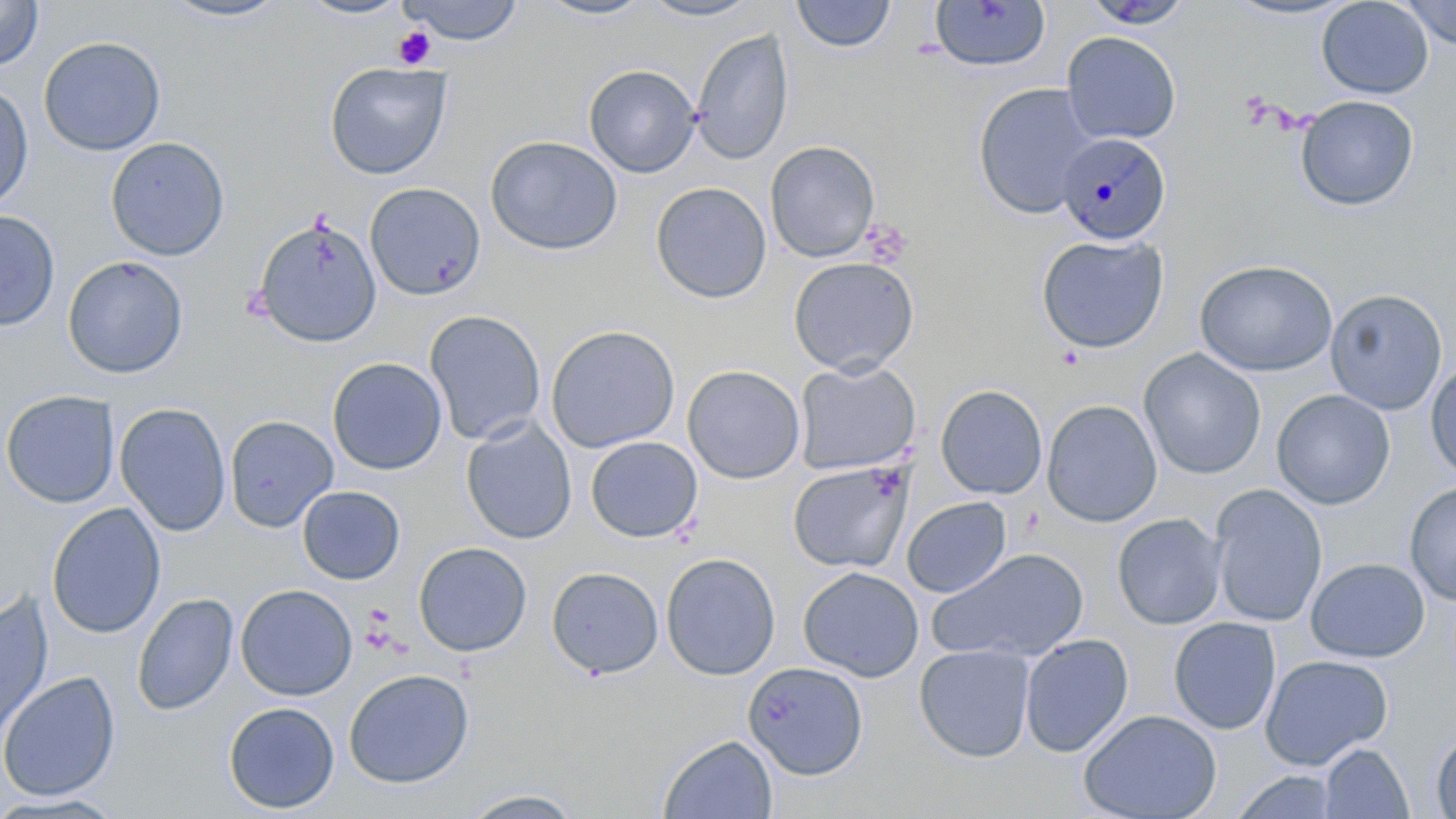

Summary:
  - Coordinate format: approximate bounding boxes as [x1, y1, x2, y2] in pixels
  - Platelet locations: [392, 26, 436, 70], [864, 220, 912, 266], [361, 609, 397, 653]
  - Uninfected red blood cell locations: [296, 0, 411, 20], [1220, 0, 1360, 22], [1317, 0, 1434, 99], [0, 1, 44, 71], [156, 1, 294, 23], [398, 1, 525, 45], [531, 1, 655, 22], [637, 1, 763, 22], [791, 1, 898, 54], [1080, 1, 1196, 29], [928, 2, 1052, 73], [1402, 2, 1456, 48], [691, 27, 794, 165], [1061, 31, 1182, 145], [38, 35, 166, 156], [324, 61, 452, 179], [583, 63, 701, 178], [0, 81, 34, 213], [973, 83, 1098, 220], [1295, 95, 1419, 211], [485, 135, 623, 255], [105, 136, 230, 261], [765, 141, 880, 262], [650, 181, 772, 304], [364, 182, 485, 301], [0, 210, 60, 332], [252, 216, 383, 349], [1036, 233, 1169, 354], [63, 255, 188, 378], [787, 256, 920, 376], [1195, 259, 1338, 377], [1325, 288, 1448, 415], [425, 310, 546, 445], [545, 324, 681, 453], [1139, 348, 1267, 480], [327, 356, 448, 475], [794, 360, 921, 475], [1425, 360, 1456, 482], [682, 364, 805, 484], [935, 384, 1048, 500], [1271, 389, 1395, 509], [1, 390, 120, 508], [1042, 399, 1162, 527], [115, 403, 231, 536], [224, 415, 339, 532], [461, 418, 577, 545], [585, 436, 703, 543], [787, 460, 913, 574], [1405, 482, 1456, 606], [297, 485, 405, 585], [1209, 485, 1327, 628], [901, 496, 1011, 598], [47, 502, 166, 639], [1112, 513, 1226, 630], [413, 541, 532, 657], [928, 548, 1089, 665], [661, 552, 781, 680], [1306, 558, 1430, 663], [546, 565, 664, 679], [798, 565, 924, 682], [235, 583, 357, 701], [0, 591, 54, 743], [132, 592, 238, 716], [1168, 617, 1281, 735], [1020, 633, 1134, 757], [914, 643, 1035, 762], [1260, 654, 1393, 770], [742, 662, 869, 780], [343, 668, 474, 788], [0, 671, 121, 802], [223, 701, 340, 814], [1079, 709, 1222, 819], [1430, 728, 1456, 819], [659, 734, 778, 819], [1319, 743, 1414, 818], [1230, 770, 1340, 818], [459, 789, 587, 818], [0, 793, 127, 818]
  - Plasmodium malariae-infected red blood cell locations: [1056, 130, 1172, 244]
  - Slide-level diagnosis: Plasmodium malariae
  - Image size: 1456×819 pixels
  - Magnification: 1000x
  - Modality: optical microscopy
  - Field of view: one of a larger specimen
  - Preparation: thin blood smear
  - Stain: May-Grünwald-Giemsa